Report the malaria status of this cell.
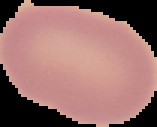

It is uninfected.

image type = segmented cell region with the area outside set to black
preparation = thin blood smear
image size = 157×127 pixels